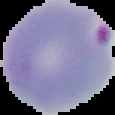

image type = segmented cell region with the area outside set to black
image size = 115×115 pixels
malaria status = parasitized
preparation = thin blood smear